Locate every blood parasite and identify its species.
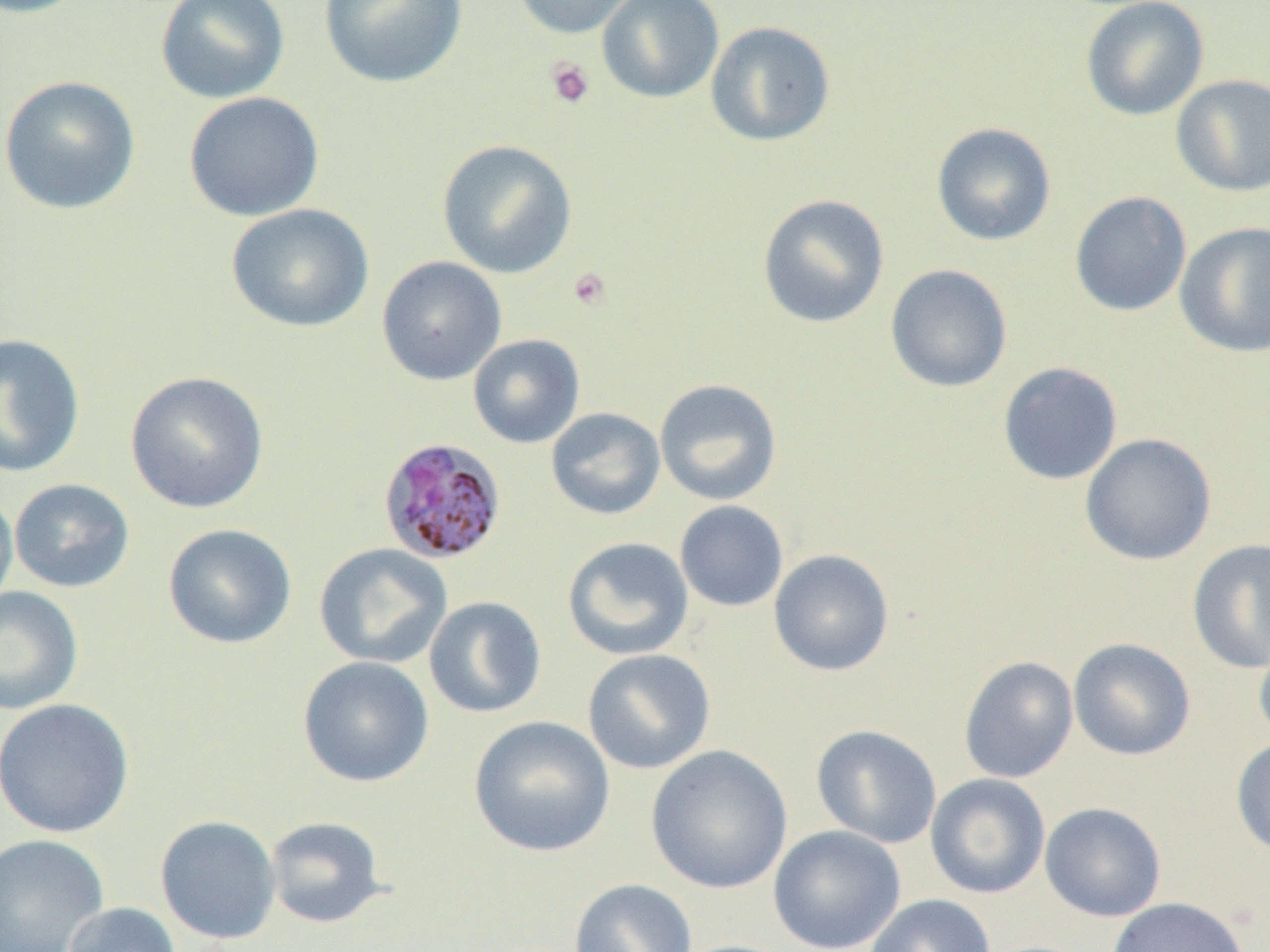
Approximate bounding boxes as [x1, y1, x2, y2] in pixels.
Plasmodium malariae-infected red blood cells: [377, 437, 508, 565].
No Plasmodium falciparum, Plasmodium ovale, Plasmodium vivax, Babesia divergens, or Trypanosoma brucei observed.

Uninfected red blood cell locations: [0, 0, 92, 19], [155, 0, 290, 104], [319, 0, 469, 88], [511, 0, 645, 39], [597, 0, 725, 104], [1080, 0, 1209, 121], [705, 20, 836, 147], [1171, 74, 1270, 196], [0, 75, 141, 215], [184, 91, 325, 222], [931, 122, 1056, 246], [437, 139, 578, 279], [1070, 191, 1192, 317], [757, 194, 890, 329], [226, 203, 374, 333], [1175, 221, 1270, 358], [376, 256, 507, 386], [885, 264, 1013, 393], [0, 333, 86, 478], [468, 333, 585, 449], [997, 361, 1123, 485], [125, 370, 270, 513], [654, 378, 782, 505], [546, 407, 666, 520], [1079, 433, 1217, 566], [9, 478, 135, 593], [0, 485, 18, 612], [675, 500, 788, 612], [162, 523, 297, 650], [562, 536, 694, 660], [1187, 538, 1270, 673], [314, 543, 452, 668], [769, 549, 895, 676], [0, 586, 83, 715], [423, 596, 547, 719], [1254, 630, 1270, 748], [1068, 638, 1196, 761], [582, 648, 716, 774], [297, 655, 435, 788], [959, 655, 1079, 784], [0, 698, 135, 838], [469, 715, 616, 858], [811, 725, 942, 848], [1231, 737, 1270, 858], [646, 744, 793, 895], [925, 773, 1051, 899], [1040, 802, 1165, 921], [155, 814, 281, 945], [265, 816, 389, 929], [768, 825, 906, 952], [0, 833, 109, 952], [569, 878, 698, 952], [864, 894, 996, 952], [1107, 896, 1249, 952], [62, 901, 182, 952]. Platelet locations: [545, 57, 595, 109], [568, 267, 612, 311]. Slide-level diagnosis: Plasmodium malariae. One field of a larger specimen. Light microscopy. 1000x magnification. Image is 1270×952 pixels. Thin blood smear.